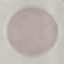
Result: no malaria parasites seen. Acquired by smartphone through the microscope eyepiece. Thin blood film. Giemsa-stained preparation. Cell patch, automatically extracted from a larger field of view and resized to 64 × 64 pixels.